Assess this cell for malaria.
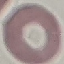
It is uninfected.

image type = automatically extracted cell patch, resized to 64 × 64 pixels
stain = Giemsa
preparation = thin blood smear
capture = smartphone camera at the microscope eyepiece